Assess the morphology of the red blood cells.
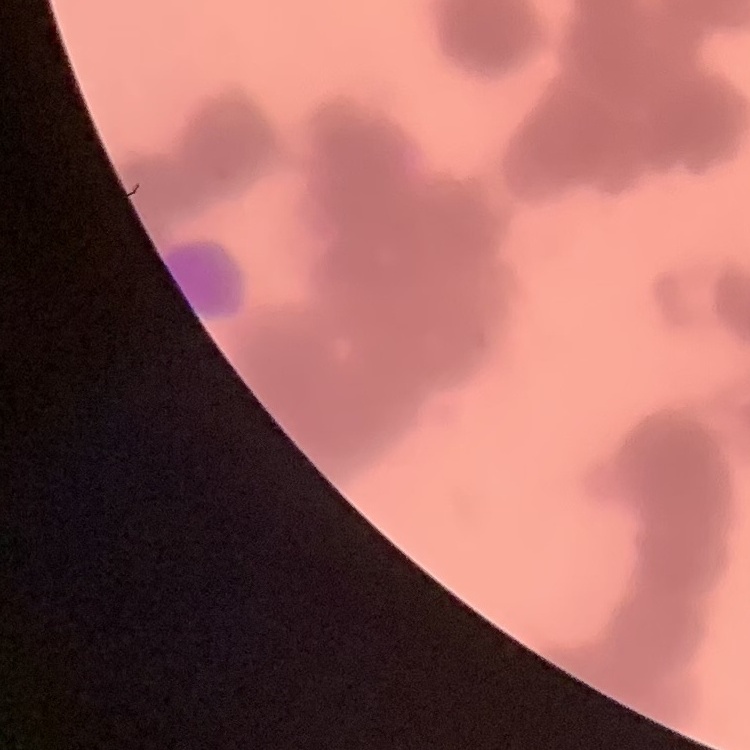

They show rouleaux formation.

One tile cut from a larger photomicrograph. Stained with either Field's or Giemsa. Thin peripheral smear.